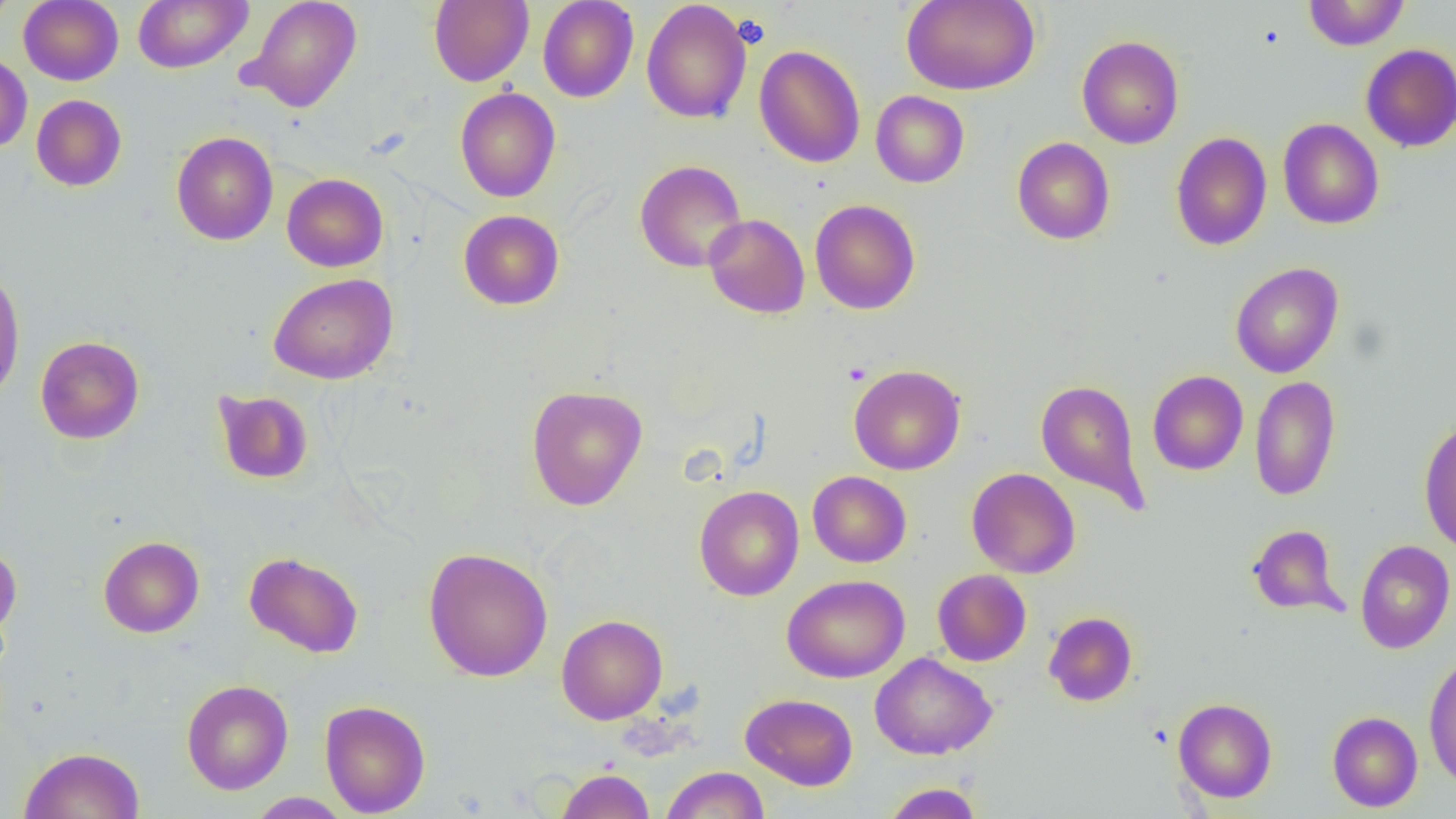
slide-level diagnosis = no evidence of blood parasites
field of view = one of a larger specimen
preparation = thin blood smear
platelet locations = approximate bounding boxes as (x1, y1, x2, y2) in pixels: (732, 14, 771, 48)
magnification = 1000x
image size = 1456×819 pixels
modality = optical microscopy
uninfected red blood cell locations = approximate bounding boxes as (x1, y1, x2, y2) in pixels: (0, 0, 17, 31), (19, 0, 123, 85), (133, 0, 252, 73), (241, 0, 362, 113), (429, 0, 533, 86), (538, 0, 638, 102), (902, 0, 1039, 95), (1303, 0, 1410, 50), (641, 1, 752, 124), (1077, 35, 1184, 149), (753, 44, 866, 168), (1360, 44, 1456, 152), (0, 52, 32, 153), (455, 86, 561, 203), (871, 91, 969, 187), (31, 94, 127, 191), (1277, 118, 1384, 230), (171, 131, 278, 245), (1170, 132, 1272, 251), (1012, 137, 1115, 245), (634, 159, 747, 272), (282, 173, 388, 272), (810, 198, 921, 315), (458, 209, 564, 310), (703, 213, 810, 319), (1230, 262, 1343, 378), (0, 265, 26, 404), (268, 273, 398, 385), (34, 335, 145, 444), (849, 364, 965, 475), (1147, 370, 1248, 475), (1249, 375, 1341, 501), (1035, 379, 1150, 514), (526, 385, 648, 510), (213, 389, 314, 484), (1418, 417, 1456, 554), (966, 467, 1080, 578), (808, 471, 911, 567), (693, 485, 804, 601), (1247, 524, 1347, 617), (98, 536, 204, 637), (1355, 539, 1455, 654), (0, 545, 22, 640), (423, 547, 553, 682), (244, 551, 364, 657), (933, 569, 1031, 666), (782, 574, 909, 683), (1044, 611, 1138, 706), (556, 614, 668, 724), (870, 652, 997, 759), (1423, 652, 1456, 789), (181, 679, 293, 794), (740, 693, 858, 790), (1173, 697, 1277, 802), (319, 699, 430, 817), (1327, 711, 1423, 812), (19, 746, 145, 819), (661, 766, 770, 819), (556, 767, 655, 819), (881, 782, 984, 819), (248, 792, 353, 818)